State the preparation type.
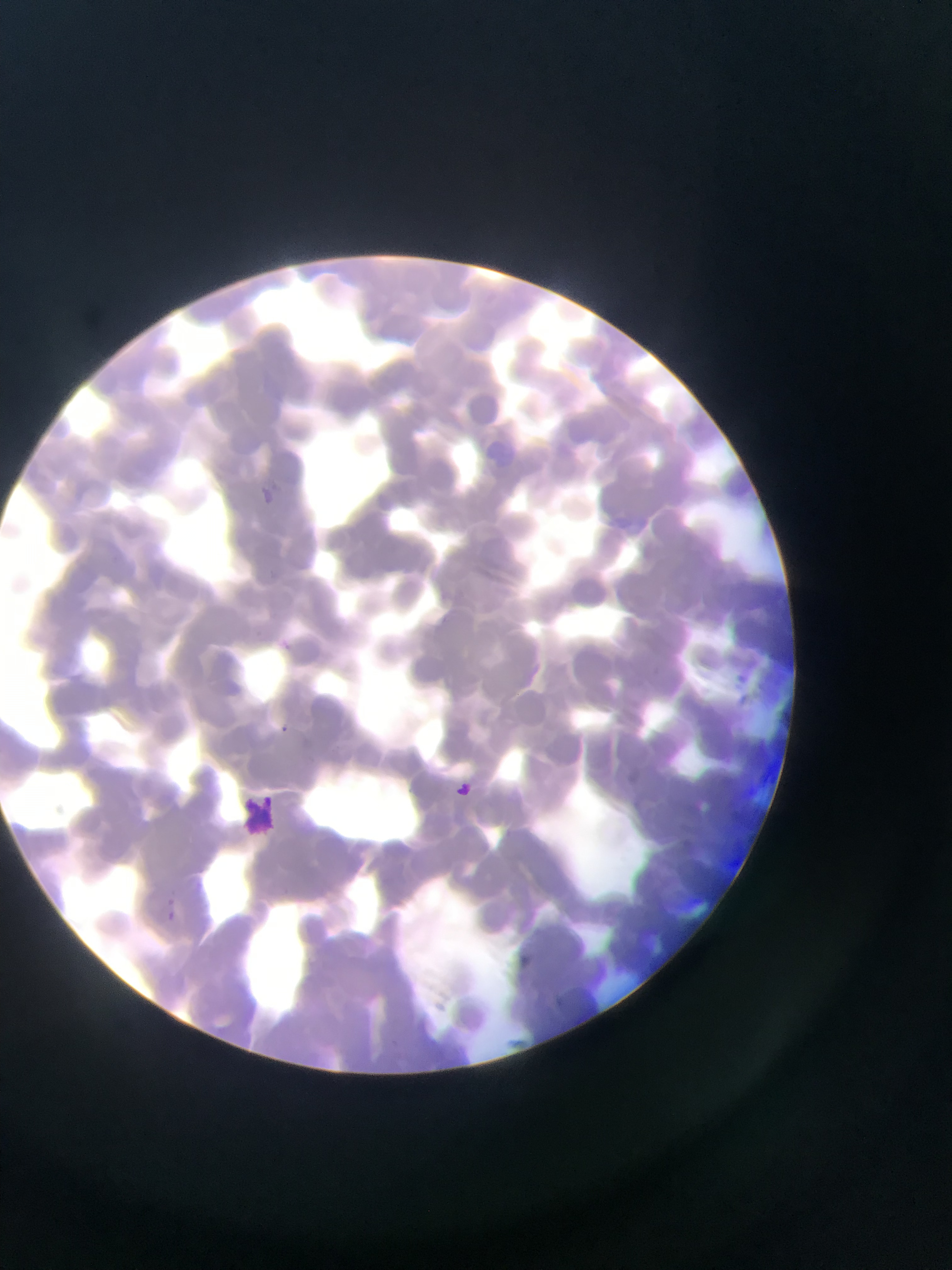
Thin blood film.

Approximate bounding boxes as (left, top, right, bottom) in pixels. Malaria parasite locations: (260, 484, 280, 501), (731, 669, 751, 687), (278, 721, 291, 737), (446, 775, 481, 808), (153, 898, 185, 930). Leukocyte locations: (238, 793, 285, 834). Photographed through a microscope with a mobile-phone camera. Image is 952×1270 pixels. Sample from Ghana. One field of view.